Assess this cell for malaria.
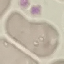

Uninfected.

Cell patch, automatically extracted from a larger field of view and resized to 64 × 64 pixels. Acquired by smartphone through the microscope eyepiece. Thin blood film. Giemsa-stained preparation.